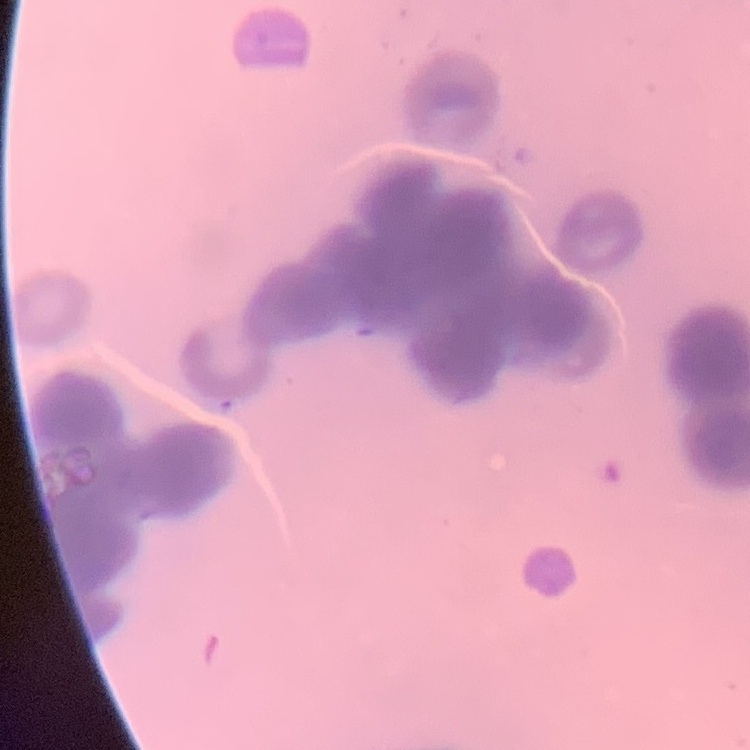
The red blood cells exhibit rouleaux formation. Thin peripheral smear. One tile cut from a larger photomicrograph. Field's or Giemsa stain.